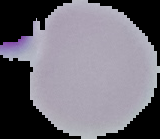

From a thin blood smear. Image is 160×139 pixels. The area outside the segmented cell region is set to black. Malaria status: uninfected.